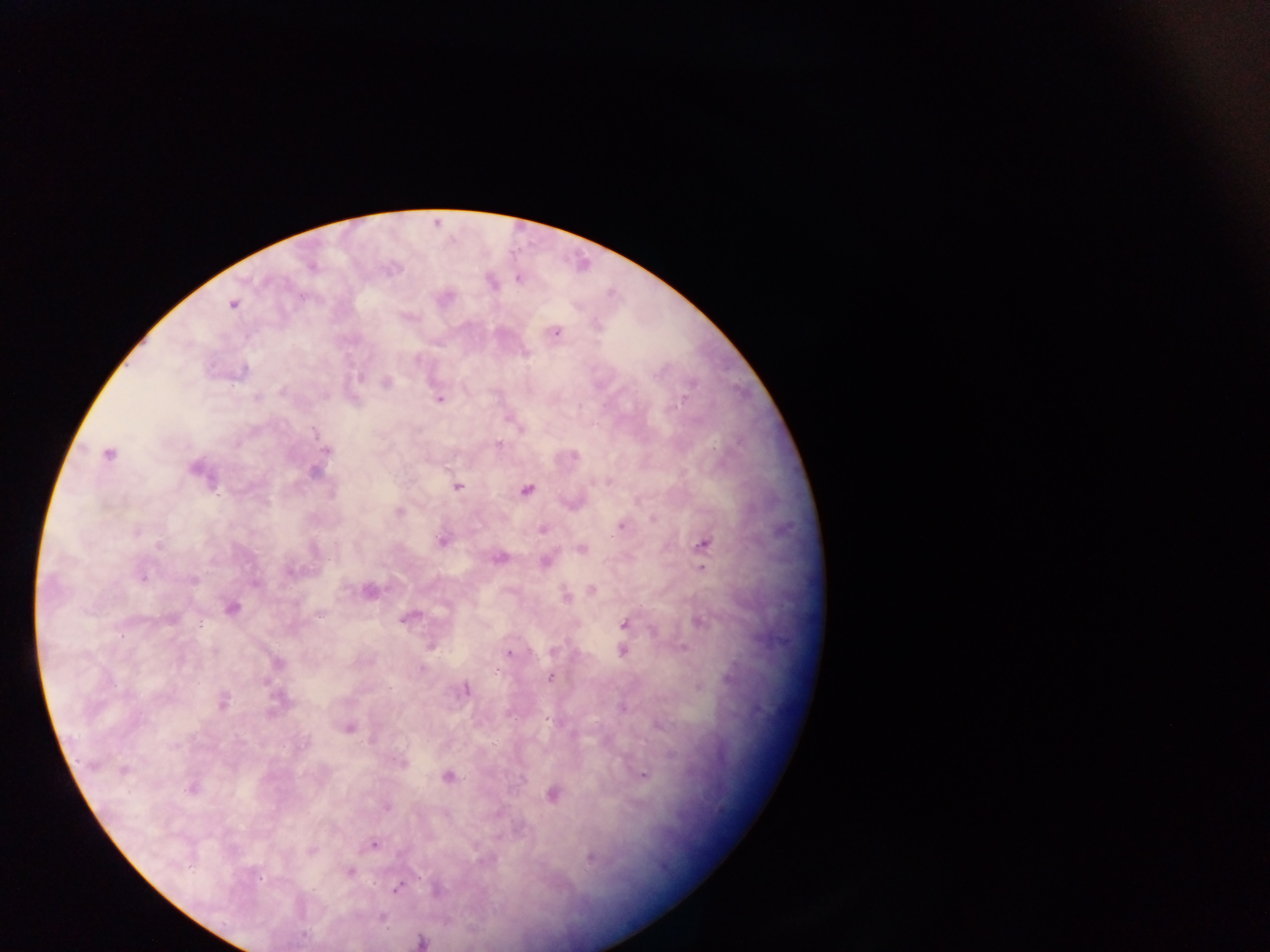

Approximate centers as {x, y} in pixels.
Summary:
  - Malaria parasite locations: {519, 278}, {233, 304}, {556, 332}, {360, 378}, {386, 382}, {281, 392}, {257, 398}, {439, 399}, {682, 400}, {314, 433}, {497, 445}, {327, 451}, {109, 455}, {194, 469}, {313, 472}, {457, 486}, {527, 490}, {399, 512}, {621, 526}, {543, 530}, {136, 531}, {442, 542}, {704, 545}, {159, 547}, {581, 549}, {500, 558}, {544, 562}, {703, 569}, {288, 572}, {142, 577}, {194, 580}, {591, 589}, {566, 598}, {231, 608}, {320, 615}, {172, 618}, {404, 619}, {701, 622}, {624, 624}, {553, 651}, {622, 651}, {215, 652}, {509, 653}, {278, 663}, {495, 670}, {550, 677}, {265, 682}, {466, 690}, {223, 703}, {622, 708}, {350, 728}, {400, 763}, {124, 770}, {643, 776}, {448, 777}, {193, 788}, {552, 795}, {386, 807}, {374, 844}, {311, 850}, {590, 858}, {350, 871}, {258, 878}, {396, 889}, {422, 942}
  - Field of view: single
  - Image size: 1270×952 pixels
  - Country: Ghana
  - Preparation: thick blood smear
  - Capture: mobile-phone photograph through a microscope